Comment on the morphology of the red blood cells.
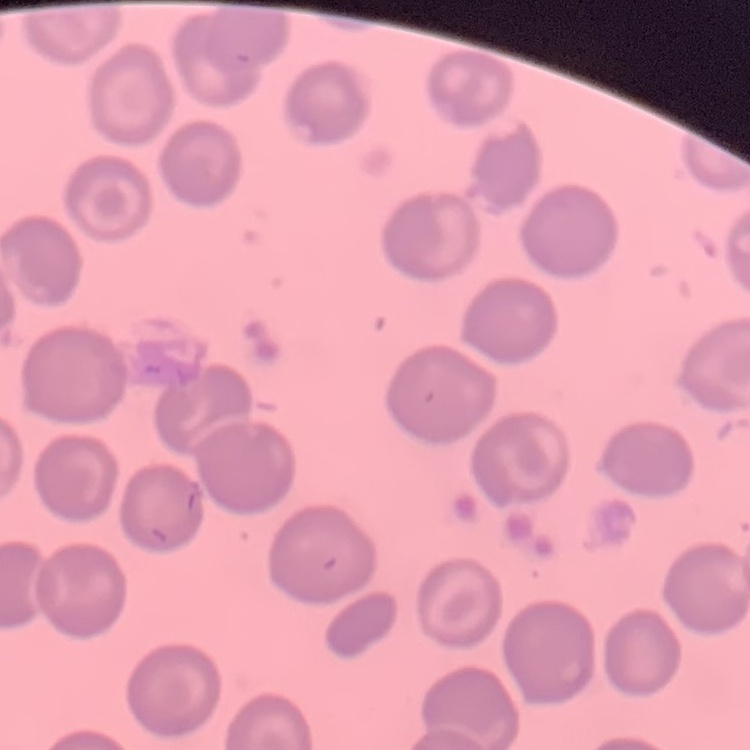
They show no rouleaux formation.

Field's or Giemsa stain. Thin blood film. One tile cut from a larger photomicrograph.